Describe the morphology of the red blood cells.
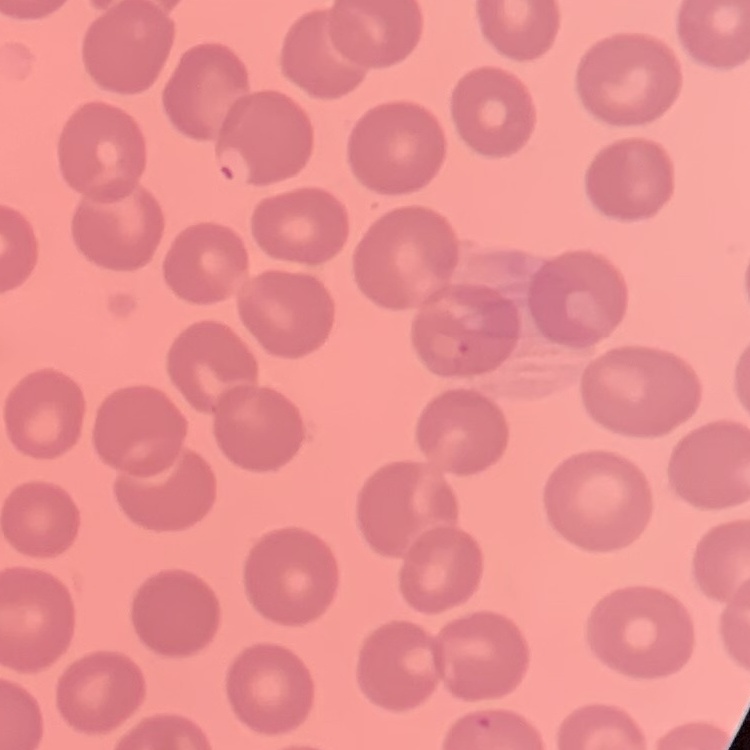
No rouleaux formation.

stain = Field's or Giemsa
preparation = thin peripheral smear
image type = one tile cut from a larger photomicrograph